Outline each blood parasite and name the species.
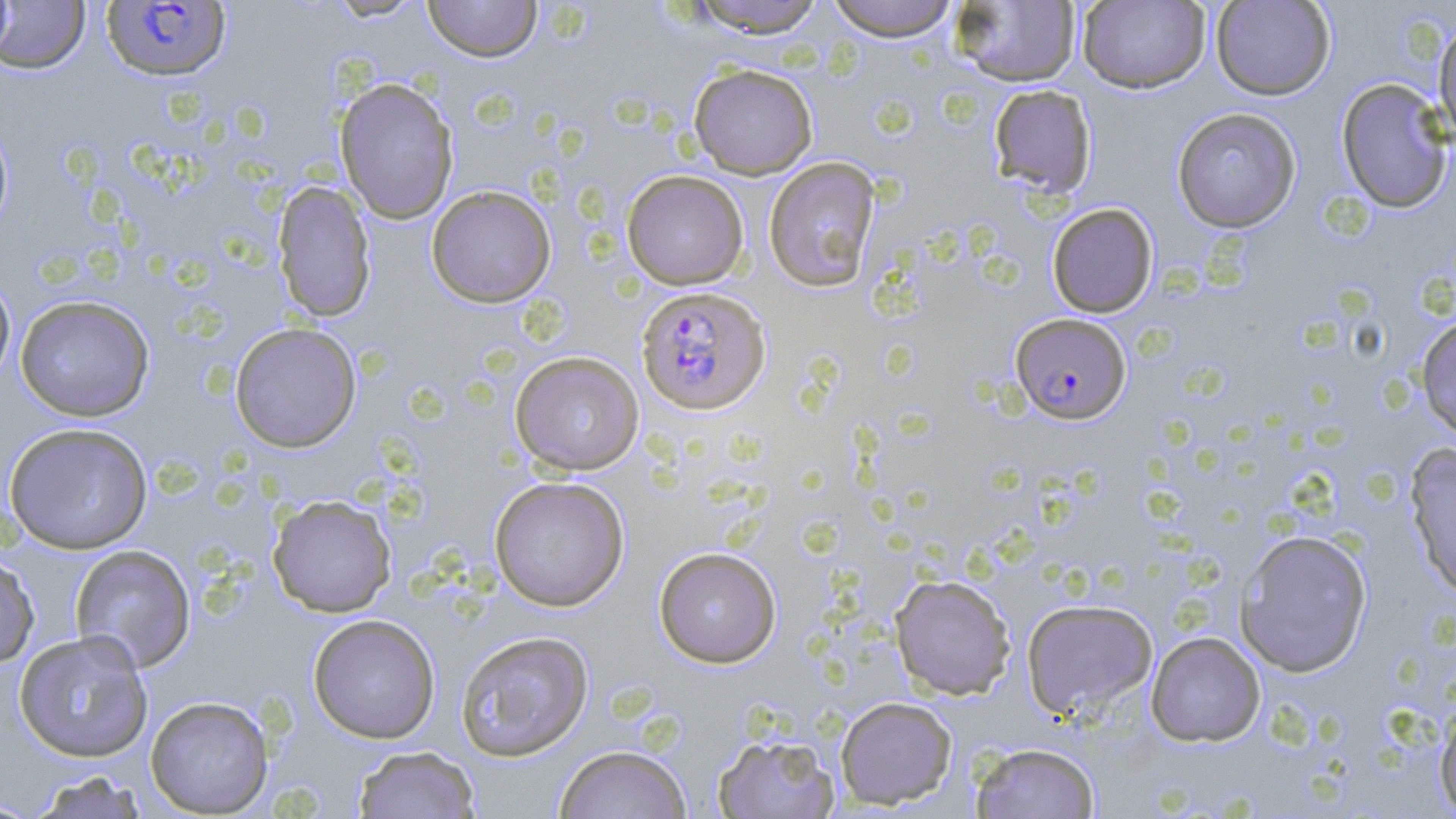

Approximate bounding boxes as named x1/y1/x2/y2 corners in pixels.
Plasmodium falciparum-infected red blood cells: (x1=102, y1=2, x2=231, y2=81), (x1=636, y1=285, x2=771, y2=415), (x1=1010, y1=312, x2=1131, y2=424).
No Plasmodium ovale, Plasmodium malariae, Plasmodium vivax, Babesia divergens, or Trypanosoma brucei observed.

Summary:
  - Uninfected red blood cell locations: (x1=0, y1=0, x2=15, y2=62), (x1=324, y1=0, x2=430, y2=23), (x1=423, y1=0, x2=542, y2=62), (x1=687, y1=0, x2=828, y2=38), (x1=824, y1=0, x2=961, y2=41), (x1=950, y1=0, x2=1081, y2=87), (x1=1077, y1=0, x2=1211, y2=94), (x1=1211, y1=0, x2=1335, y2=100), (x1=0, y1=1, x2=91, y2=74), (x1=1433, y1=17, x2=1456, y2=144), (x1=688, y1=63, x2=818, y2=179), (x1=334, y1=76, x2=459, y2=224), (x1=1335, y1=78, x2=1453, y2=213), (x1=988, y1=84, x2=1098, y2=200), (x1=1171, y1=107, x2=1302, y2=232), (x1=0, y1=113, x2=14, y2=238), (x1=763, y1=157, x2=881, y2=293), (x1=621, y1=170, x2=749, y2=290), (x1=273, y1=180, x2=375, y2=322), (x1=426, y1=185, x2=557, y2=308), (x1=1046, y1=203, x2=1158, y2=318), (x1=0, y1=271, x2=16, y2=392), (x1=15, y1=295, x2=155, y2=421), (x1=1415, y1=314, x2=1456, y2=442), (x1=229, y1=322, x2=362, y2=453), (x1=509, y1=351, x2=644, y2=475), (x1=3, y1=421, x2=153, y2=554), (x1=1404, y1=442, x2=1456, y2=598), (x1=489, y1=476, x2=630, y2=611), (x1=267, y1=494, x2=397, y2=617), (x1=1235, y1=529, x2=1373, y2=677), (x1=69, y1=545, x2=196, y2=672), (x1=654, y1=546, x2=782, y2=668), (x1=0, y1=550, x2=40, y2=668), (x1=889, y1=574, x2=1016, y2=700), (x1=1020, y1=598, x2=1158, y2=720), (x1=307, y1=613, x2=441, y2=743), (x1=13, y1=630, x2=154, y2=762), (x1=455, y1=630, x2=594, y2=761), (x1=1145, y1=631, x2=1266, y2=747), (x1=145, y1=695, x2=274, y2=817), (x1=834, y1=696, x2=958, y2=810), (x1=1433, y1=700, x2=1456, y2=816), (x1=711, y1=731, x2=841, y2=818), (x1=969, y1=742, x2=1101, y2=818), (x1=554, y1=744, x2=692, y2=818), (x1=352, y1=745, x2=481, y2=818), (x1=27, y1=770, x2=149, y2=819), (x1=0, y1=796, x2=44, y2=817)
  - Slide-level diagnosis: Plasmodium falciparum
  - Stain: May-Grünwald-Giemsa
  - Preparation: thin blood film
  - Magnification: 1000x
  - Modality: optical microscopy
  - Field of view: single
  - Image size: 1456×819 pixels